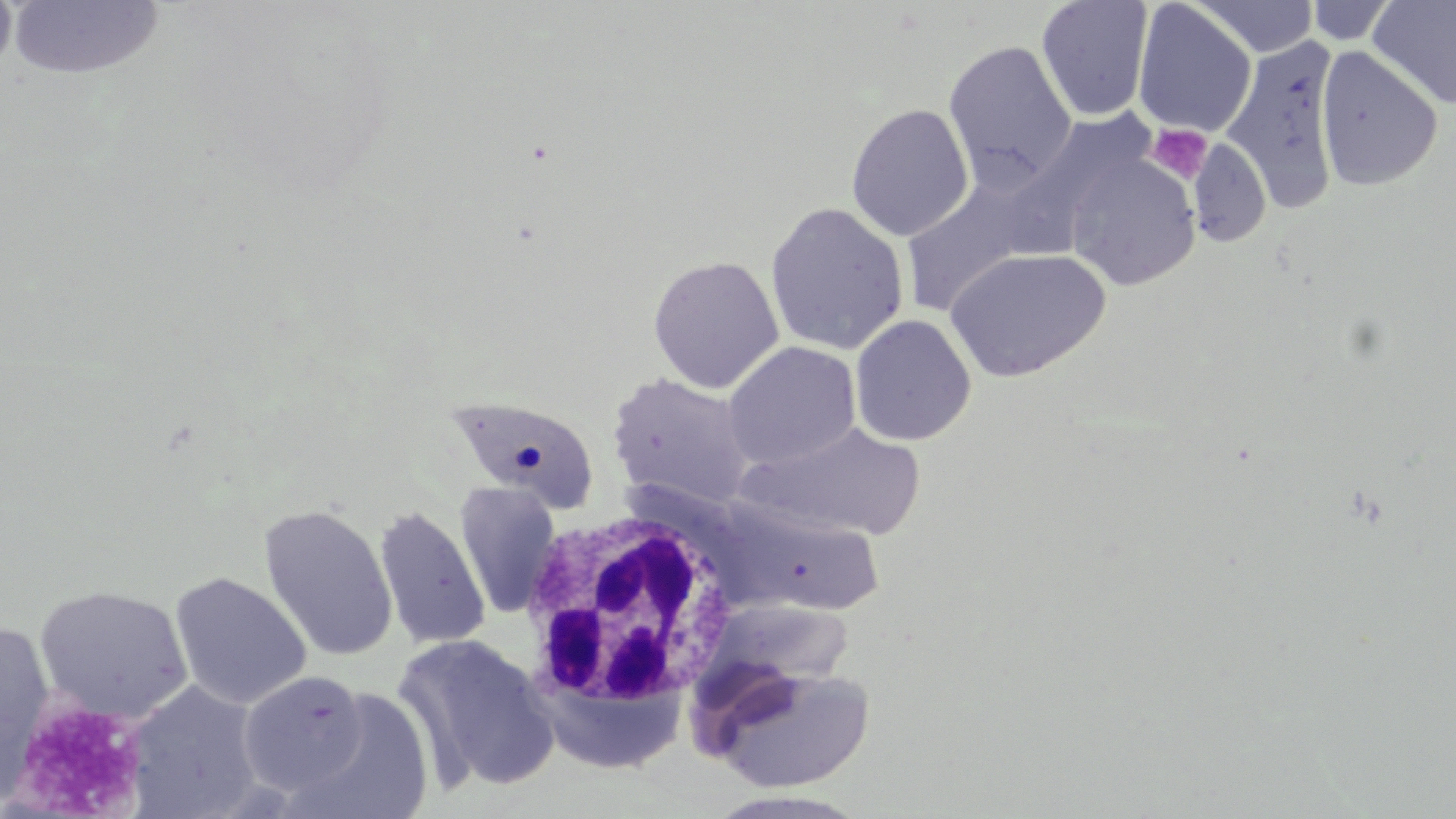

Summary:
  - Coordinate format: approximate bounding boxes as [x1, y1, x2, y2] in pixels
  - Uninfected red blood cell locations: [0, 0, 17, 82], [8, 0, 164, 82], [1188, 0, 1319, 58], [1036, 1, 1155, 121], [1132, 1, 1258, 138], [1304, 1, 1398, 45], [1369, 1, 1456, 110], [1221, 34, 1343, 214], [943, 40, 1076, 187], [1315, 46, 1442, 191], [845, 104, 974, 242], [1188, 136, 1272, 248], [1065, 154, 1201, 290], [900, 177, 1040, 317], [764, 201, 910, 356], [945, 247, 1112, 382], [647, 255, 784, 393], [850, 314, 977, 447], [723, 341, 861, 470], [606, 372, 756, 510], [444, 400, 599, 518], [740, 420, 929, 541], [455, 482, 561, 618], [721, 502, 885, 616], [258, 503, 398, 662], [373, 506, 490, 650], [169, 571, 311, 710], [33, 584, 193, 724], [0, 621, 56, 800], [395, 634, 563, 793], [706, 663, 878, 792], [237, 670, 370, 794], [126, 681, 265, 818], [295, 689, 435, 819], [703, 790, 872, 819]
  - White blood cell locations: [518, 505, 740, 712]
  - Platelet locations: [1147, 123, 1213, 184], [6, 698, 147, 816]
  - Slide-level diagnosis: no evidence of blood parasites
  - Modality: light microscopy
  - Magnification: 1000x
  - Stain: May-Grünwald-Giemsa
  - Field of view: single
  - Preparation: thin blood film
  - Image size: 1456×819 pixels